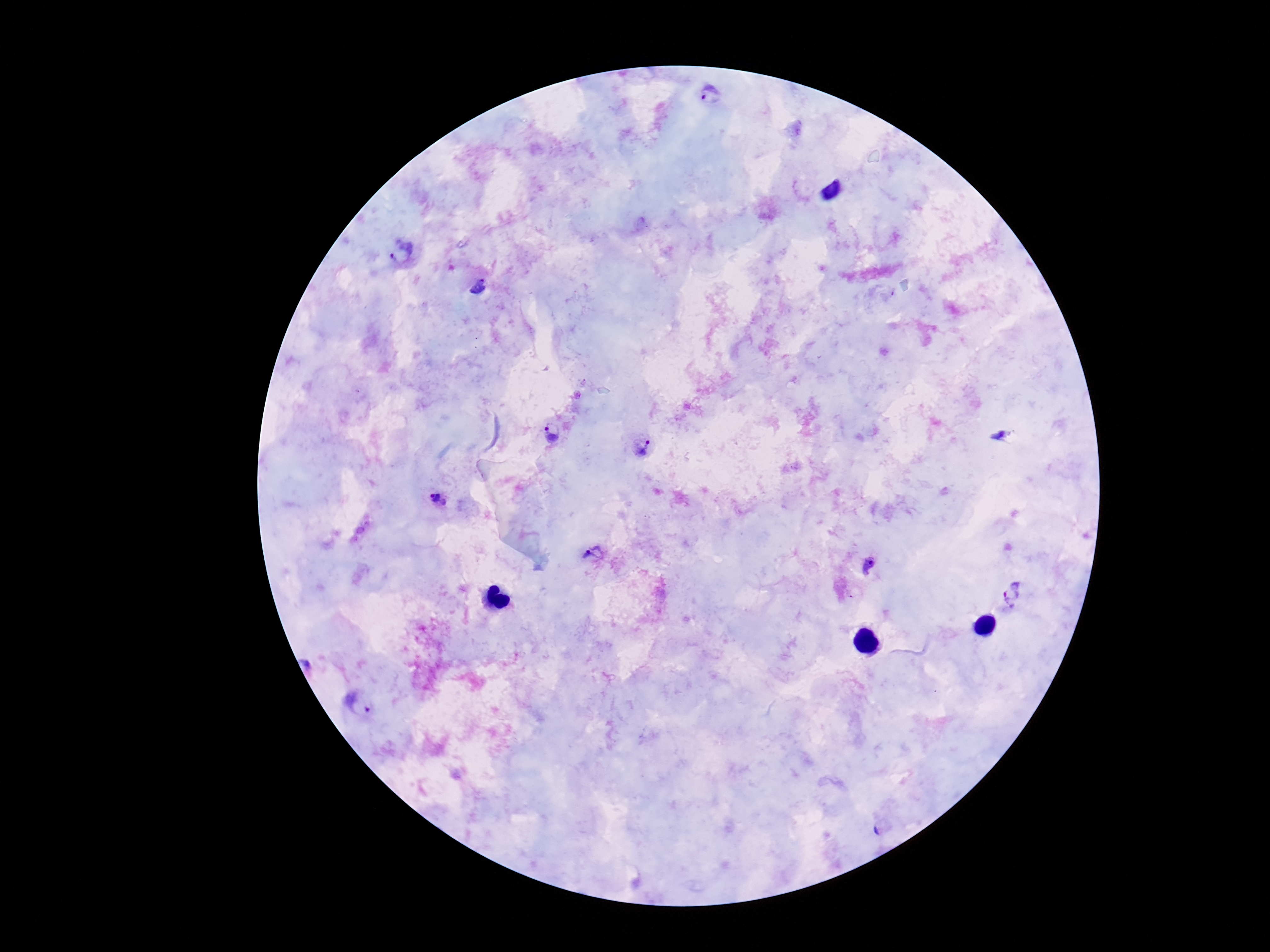
Approximate centers as {x, y} in pixels. Plasmodium parasite locations: {712, 94}, {402, 252}, {478, 287}, {553, 434}, {1003, 436}, {640, 445}, {438, 499}, {593, 556}, {870, 567}, {1012, 596}, {360, 703}. 100x magnification. Thick blood smear. Patient malaria status: positive. Giemsa-stained preparation. Smartphone photograph taken through the microscope eyepiece. Image is 1270×952 pixels. One field from this slide.